Name the cell type shown.
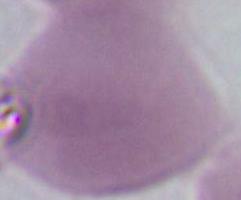
An erythrocyte.

Photomicrograph. Captured at 1000x magnification.